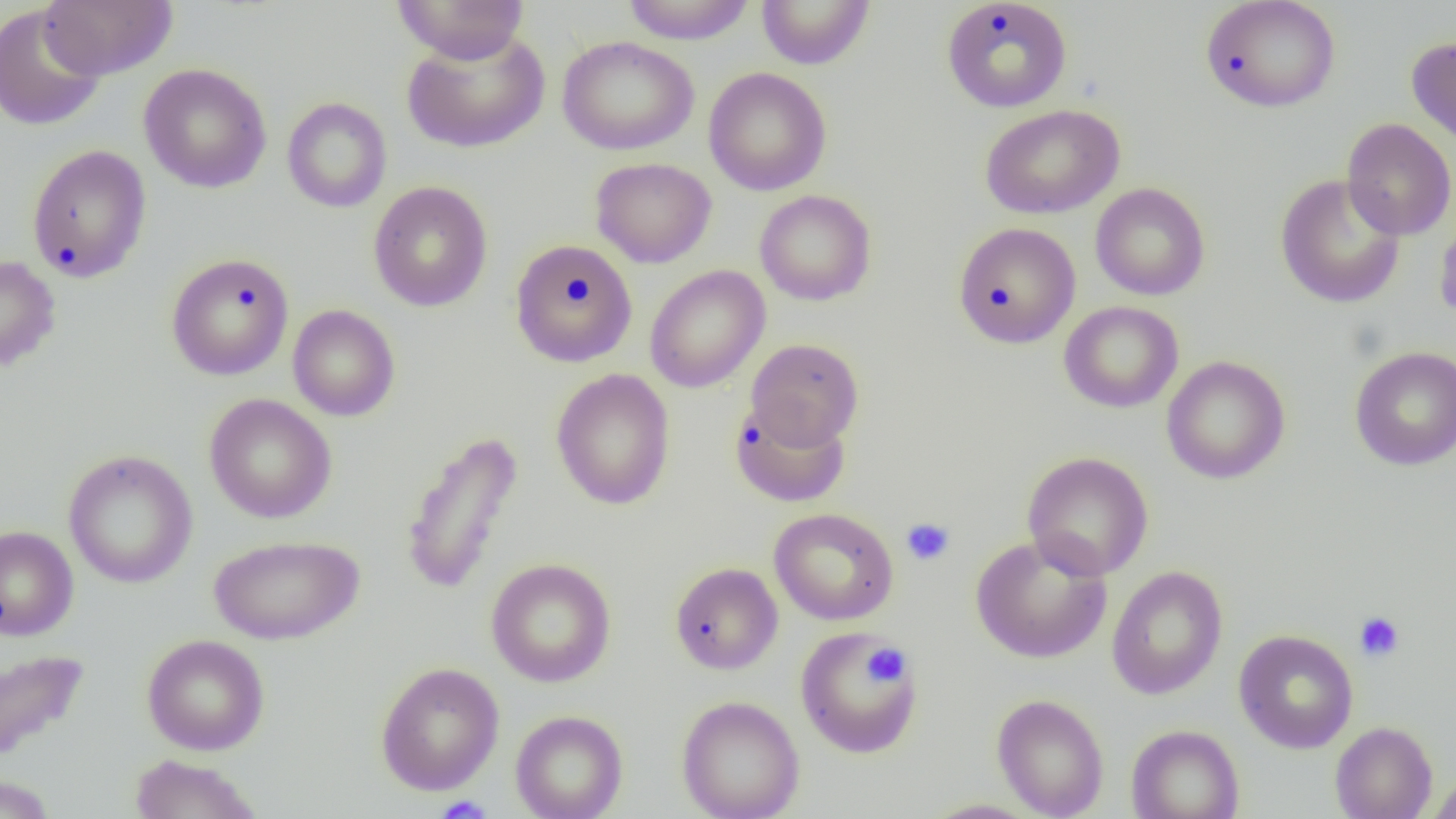 Approximate bounding boxes as (x1,y1)-(x2,y2) corner pairs in pixels. Uninfected red blood cell locations: (392,0)-(529,64), (621,0)-(758,45), (757,0)-(875,69), (942,0)-(1073,113), (1201,0)-(1341,113), (38,1)-(178,80), (0,4)-(107,132), (401,28)-(550,154), (557,35)-(699,155), (1406,35)-(1456,151), (138,63)-(272,193), (703,67)-(832,196), (282,96)-(392,213), (980,104)-(1124,219), (1341,118)-(1456,240), (26,144)-(152,283), (590,157)-(717,268), (1275,173)-(1406,309), (368,181)-(493,312), (1090,182)-(1210,301), (754,189)-(877,306), (1434,209)-(1456,328), (953,222)-(1081,348), (509,239)-(638,367), (166,252)-(294,381), (0,255)-(61,373), (644,266)-(770,393), (1059,301)-(1184,413), (287,304)-(401,421), (746,338)-(864,449), (1349,346)-(1456,470), (1161,355)-(1291,484), (550,369)-(676,510), (204,393)-(337,524), (730,399)-(851,508), (399,429)-(524,596), (63,450)-(198,588), (1022,451)-(1154,580), (769,507)-(899,625), (0,525)-(79,641), (970,533)-(1112,664), (209,534)-(364,645), (485,557)-(616,687), (669,561)-(783,674), (1106,565)-(1228,700), (795,627)-(923,758), (1233,629)-(1359,753), (142,634)-(270,755), (0,649)-(90,765), (375,662)-(504,796), (991,693)-(1109,819), (676,695)-(804,819), (510,710)-(628,819), (1330,721)-(1437,819), (1126,725)-(1245,819), (129,754)-(262,819), (1426,773)-(1456,819), (0,774)-(57,819), (922,799)-(1043,818). Platelet locations: (900,517)-(955,566), (1354,611)-(1405,662), (864,643)-(909,686), (433,796)-(494,819). Slide-level diagnosis: no evidence of blood parasites. Single field of view. Image is 1456×819 pixels. 1000x magnification. Thin blood film. Light microscopy.